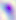 Toxoplasma gondii is seen. Captured at 400x magnification. Photomicrograph.